State which parasite is depicted.
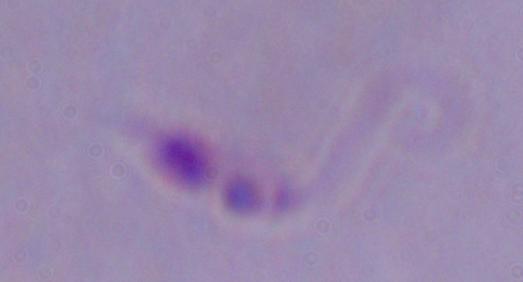
Leishmania.

magnification = 1000x
modality = photomicrograph